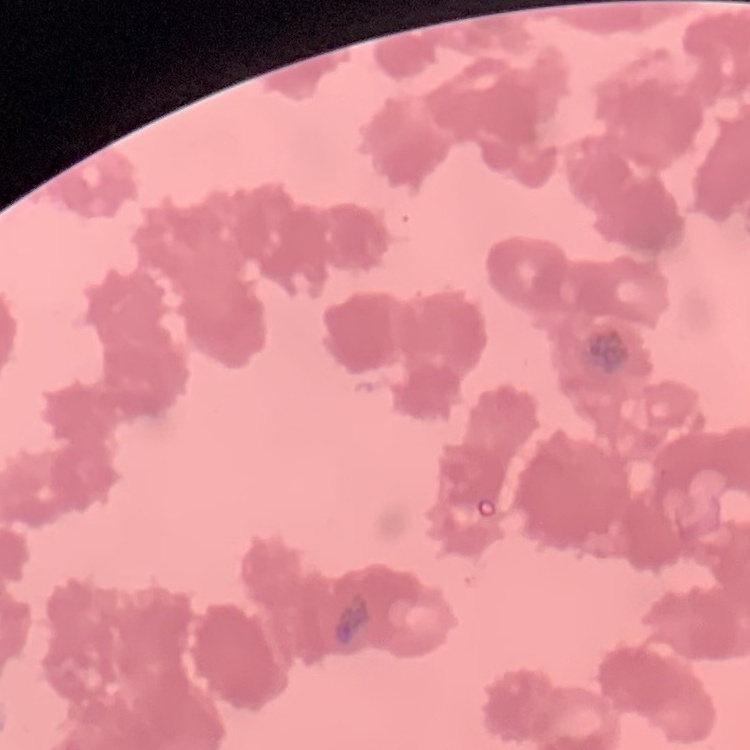

Summary:
  - Red blood cell morphology: rouleaux formation
  - Stain: Field's or Giemsa
  - Image type: square crop of a larger photomicrograph
  - Preparation: thin blood film